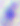

Toxoplasma gondii is seen. Captured at 400x magnification. Micrograph.